Locate every blood parasite and identify its species.
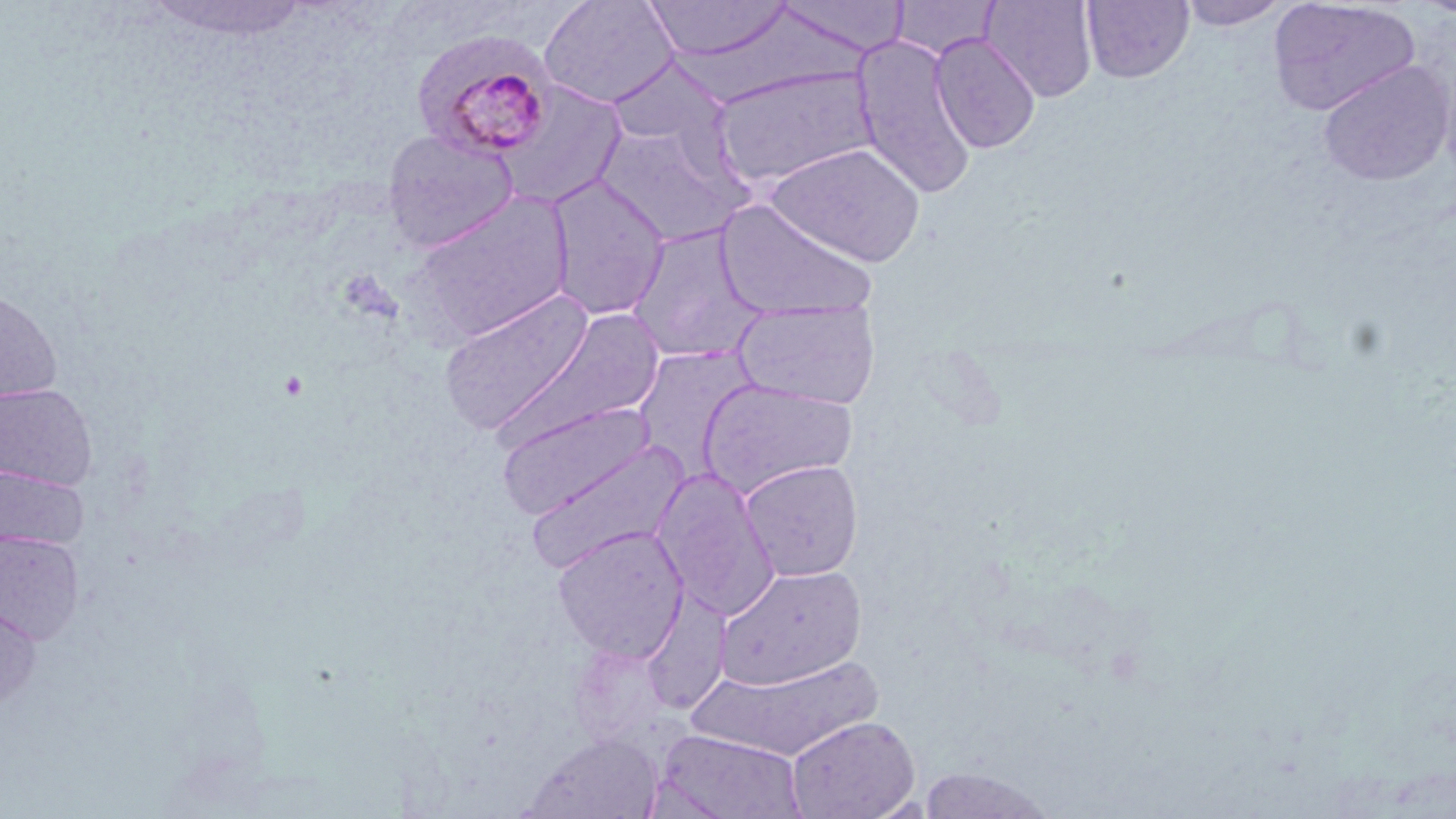
Approximate bounding boxes as (x1,y1)-(x2,y2) corner pairs in pixels.
Plasmodium malariae-infected red blood cells: (412,28)-(559,161).
No Plasmodium falciparum, Plasmodium ovale, Plasmodium vivax, Babesia divergens, or Trypanosoma brucei observed.

Uninfected red blood cell locations: (538,0)-(679,108), (642,0)-(793,63), (770,0)-(911,57), (979,0)-(1098,102), (1267,0)-(1421,116), (145,1)-(316,43), (1081,1)-(1195,83), (1178,1)-(1290,31), (930,32)-(1041,154), (852,34)-(977,200), (605,57)-(730,153), (1316,60)-(1454,186), (712,65)-(878,188), (492,81)-(628,210), (594,123)-(750,246), (382,128)-(518,252), (765,142)-(926,266), (545,175)-(671,320), (407,192)-(576,347), (714,198)-(878,322), (625,224)-(767,363), (0,287)-(63,405), (438,287)-(596,436), (732,298)-(882,410), (493,308)-(665,453), (632,345)-(760,481), (697,378)-(858,498), (0,382)-(98,489), (497,402)-(657,519), (524,438)-(692,573), (738,460)-(864,581), (0,466)-(88,551), (651,467)-(781,621), (551,526)-(689,662), (0,531)-(83,643), (717,565)-(866,690), (0,598)-(42,712), (687,653)-(884,761), (786,715)-(920,819), (654,728)-(807,819), (522,732)-(664,819), (917,766)-(1056,817). Slide-level diagnosis: Plasmodium malariae. Thin blood smear. Light microscopy. Captured at 1000x magnification. May-Grünwald-Giemsa stain. Image is 1456×819 pixels. Single field of view.